State which parasite is depicted.
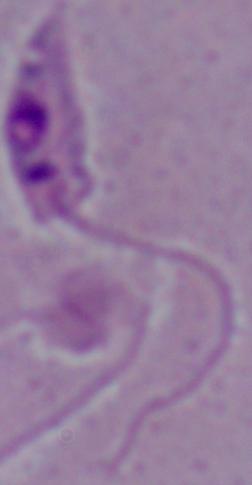

Leishmania.

Micrograph. Captured at 1000x magnification.